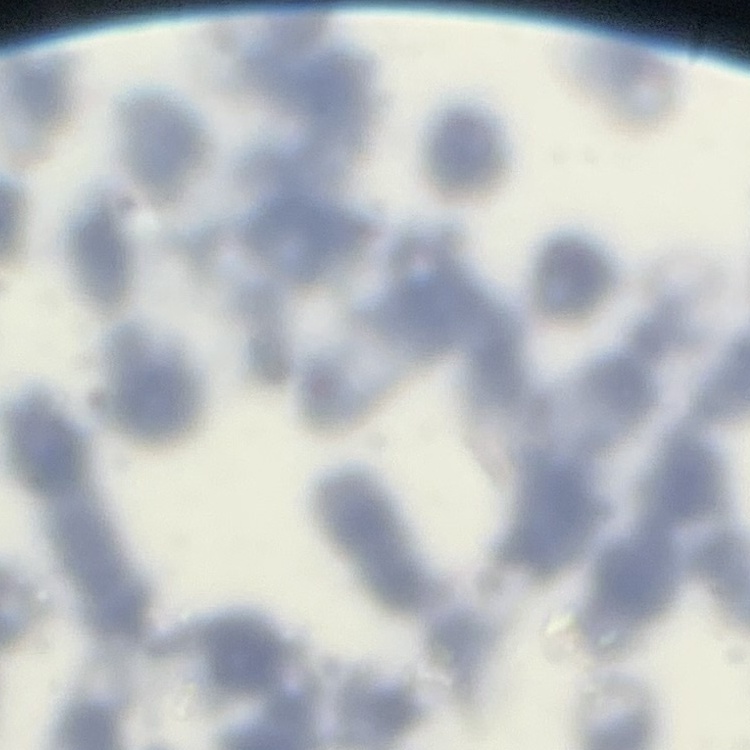

Summary:
  - Erythrocyte morphology: rouleaux formation
  - Image type: one tile cut from a larger photomicrograph
  - Preparation: thin blood film
  - Stain: Field's or Giemsa